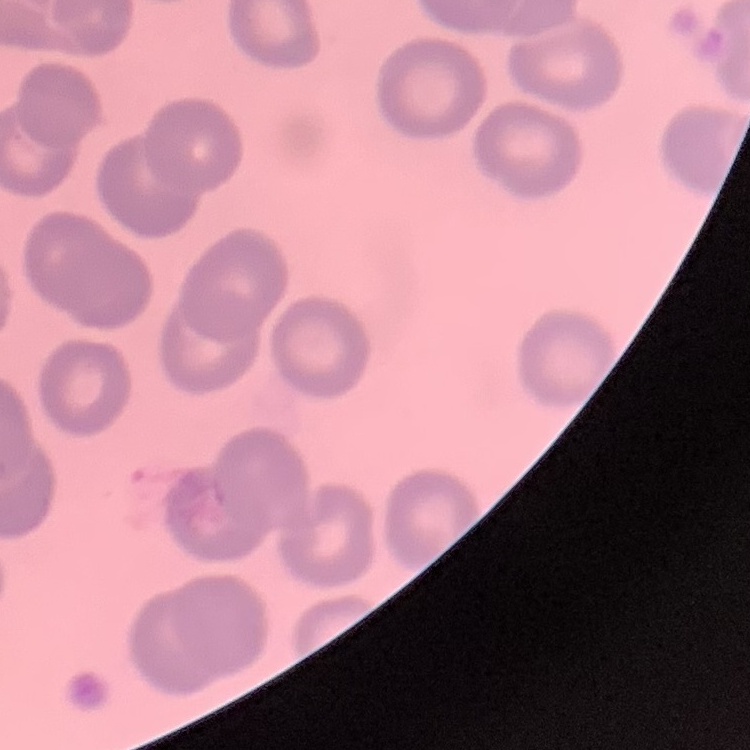
The erythrocytes show no rouleaux formation. Stained with either Field's or Giemsa. Square crop of a larger photomicrograph. Thin blood film.